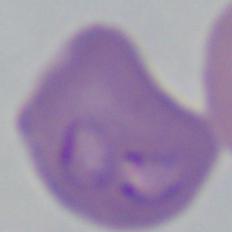

Summary:
  - Identification: Babesia
  - Magnification: 1000x
  - Modality: photomicrograph